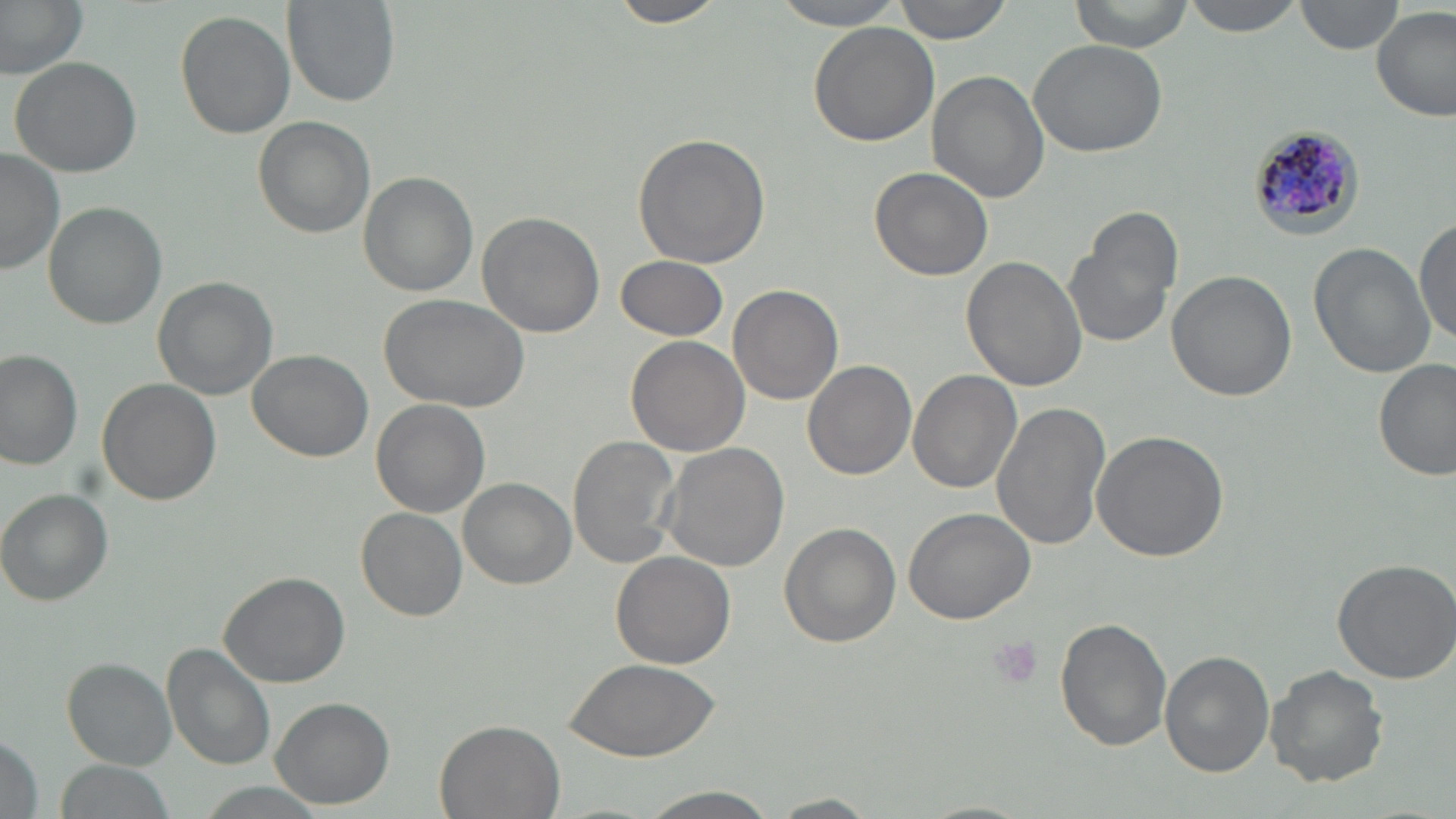
Approximate bounding boxes as [x1, y1, x2, y2] in pixels. Uninfected red blood cell locations: [0, 0, 87, 78], [283, 0, 398, 108], [607, 0, 729, 28], [771, 0, 908, 28], [893, 0, 1015, 44], [1071, 0, 1195, 53], [1180, 0, 1306, 37], [1295, 0, 1404, 55], [1373, 5, 1454, 121], [174, 8, 295, 140], [807, 25, 940, 148], [1029, 37, 1171, 156], [9, 57, 142, 178], [928, 71, 1050, 202], [253, 117, 374, 239], [632, 132, 770, 268], [1, 151, 65, 276], [869, 167, 994, 280], [357, 172, 478, 296], [43, 201, 167, 329], [1063, 210, 1183, 350], [476, 212, 604, 338], [1413, 216, 1456, 343], [1309, 244, 1432, 378], [615, 256, 729, 341], [962, 256, 1088, 393], [1164, 270, 1297, 402], [153, 277, 276, 400], [730, 284, 843, 405], [379, 293, 528, 409], [625, 336, 749, 457], [247, 350, 374, 461], [0, 351, 82, 470], [1375, 359, 1455, 482], [805, 360, 916, 480], [908, 370, 1022, 494], [96, 378, 221, 504], [371, 398, 489, 516], [990, 399, 1110, 551], [1091, 429, 1228, 561], [569, 434, 683, 568], [658, 441, 791, 572], [458, 478, 575, 588], [2, 488, 113, 604], [357, 508, 467, 620], [904, 508, 1034, 623], [777, 523, 901, 648], [611, 551, 735, 669], [1330, 558, 1456, 684], [218, 571, 349, 688], [1057, 617, 1173, 751], [164, 644, 276, 770], [1159, 650, 1272, 776], [562, 657, 719, 758], [64, 659, 178, 767], [1265, 664, 1388, 788], [269, 697, 394, 808], [434, 719, 566, 819], [0, 724, 43, 819], [55, 760, 176, 816], [191, 783, 334, 818], [634, 786, 782, 819], [770, 793, 881, 817]. Plasmodium malariae-infected red blood cell locations: [1247, 124, 1367, 244]. Platelet locations: [989, 635, 1044, 693]. Slide-level diagnosis: Plasmodium malariae. Thin blood smear. Light microscopy. Captured at 1000x magnification. One field of a larger specimen. Image is 1456×819 pixels. May-Grünwald-Giemsa stain.